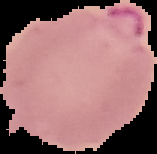
Summary:
  - Preparation: thin blood smear
  - Image size: 157×154 pixels
  - Image type: segmented cell region on a black background
  - Result: Plasmodium parasites detected